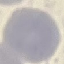
Summary:
  - Malaria status: uninfected
  - Image type: cell patch, automatically extracted from a larger field of view and resized to 64 × 64 pixels
  - Capture: smartphone camera at the microscope eyepiece
  - Stain: Giemsa
  - Preparation: thin smear